Classify this cell by malaria status.
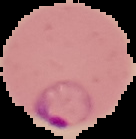
Parasitized.

image type = segmented cell region on a black background
preparation = thin blood film
image size = 136×139 pixels